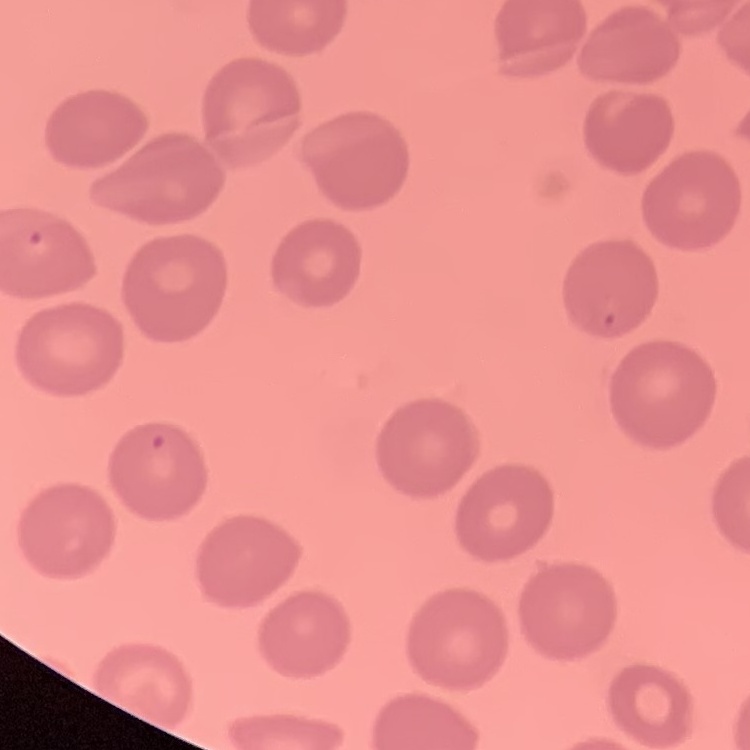

red blood cell morphology = no rouleaux formation
stain = Field's or Giemsa
image type = one tile cut from a larger photomicrograph
preparation = thin peripheral smear